Name the parasite shown.
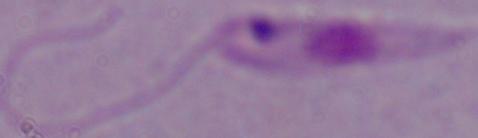
Leishmania.

magnification = 1000x
modality = micrograph